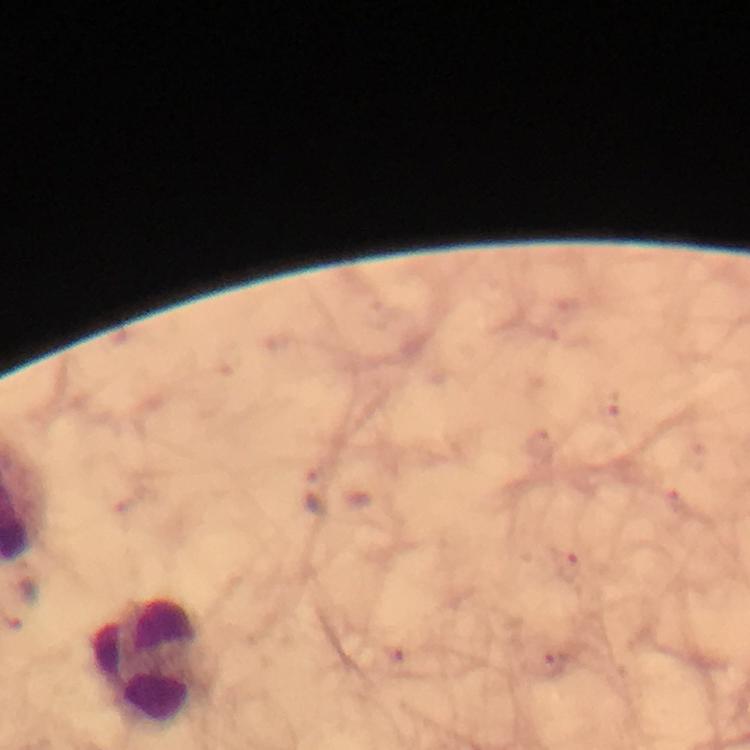
Approximate object centers, in pixels from the top-left corner. Plasmodium parasite locations: (x=315, y=492). Leukocyte locations: (x=154, y=663). Thick smear. Giemsa-stained preparation. Immersion oil applied. Image is 750×750 pixels. 100x magnification. Photographed through the microscope with a smartphone camera. Cropped region of a single field of view. From a diagnostic examination for malaria.